Locate every blood parasite and identify its species.
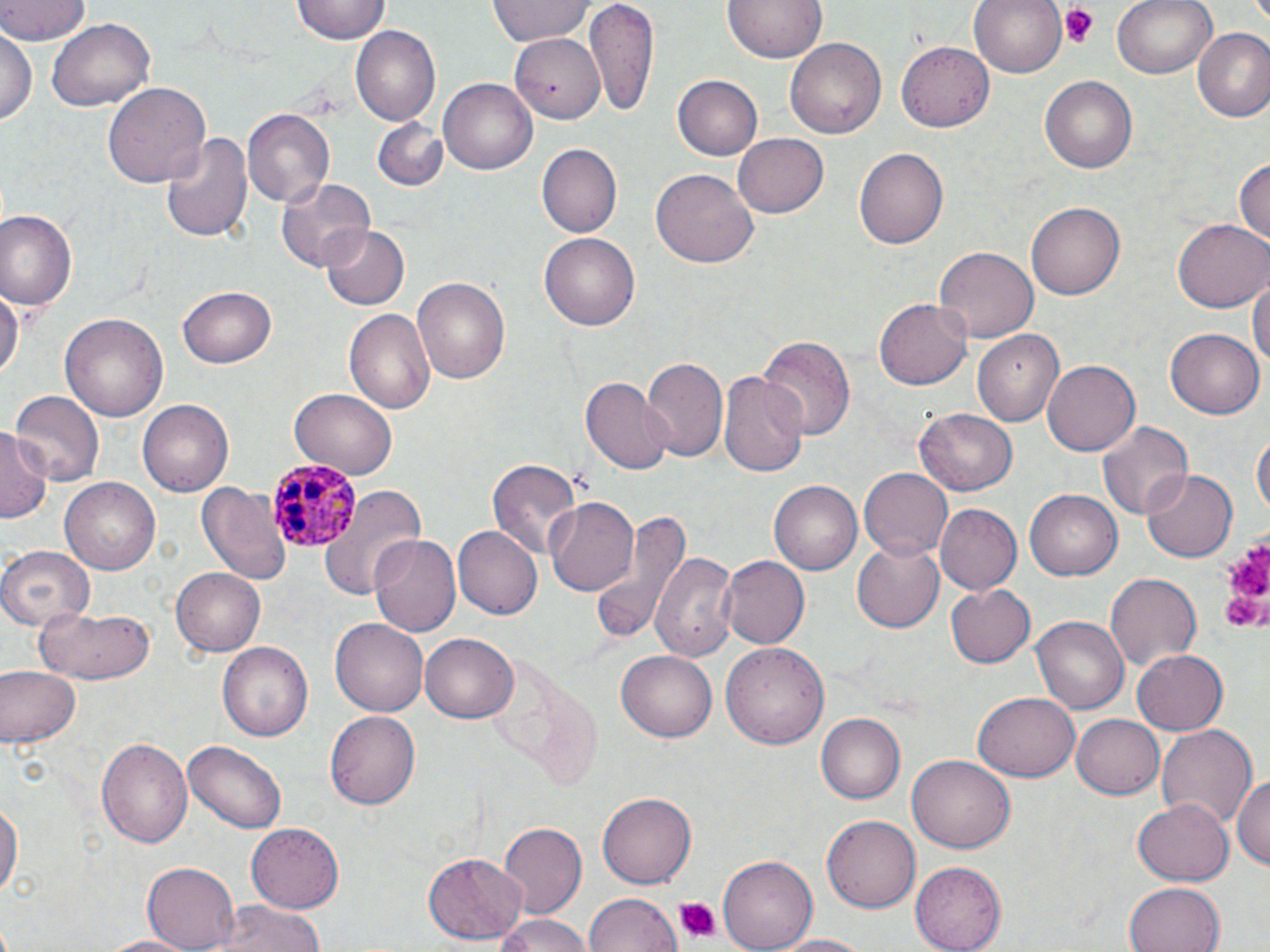

Approximate bounding boxes as (x1, y1, x2, y2) in pixels.
Plasmodium malariae-infected red blood cells: (268, 459, 363, 552).
No Plasmodium falciparum, Plasmodium ovale, Plasmodium vivax, Babesia divergens, or Trypanosoma brucei observed.

Platelet locations: (1062, 6, 1101, 46), (1217, 530, 1270, 638), (671, 895, 721, 942). Uninfected red blood cell locations: (0, 0, 92, 46), (292, 0, 390, 44), (488, 0, 592, 46), (584, 0, 659, 115), (721, 0, 828, 64), (969, 0, 1069, 79), (1113, 0, 1218, 79), (46, 17, 154, 112), (1, 24, 36, 132), (351, 26, 440, 126), (1192, 27, 1270, 123), (511, 35, 598, 124), (784, 37, 885, 140), (899, 40, 993, 131), (675, 74, 763, 160), (1041, 75, 1135, 174), (439, 78, 537, 175), (102, 82, 212, 191), (241, 109, 337, 207), (371, 118, 450, 192), (162, 128, 254, 244), (731, 134, 832, 217), (535, 143, 621, 237), (853, 147, 948, 250), (1233, 154, 1269, 250), (652, 169, 757, 270), (275, 175, 374, 272), (1025, 201, 1124, 302), (1, 210, 78, 309), (1173, 218, 1270, 313), (318, 222, 409, 309), (542, 232, 638, 331), (934, 245, 1039, 343), (1250, 271, 1270, 379), (412, 274, 511, 387), (0, 282, 21, 383), (178, 286, 276, 369), (874, 298, 972, 391), (343, 306, 436, 418), (60, 312, 169, 422), (1166, 327, 1263, 418), (973, 330, 1064, 426), (758, 334, 854, 440), (641, 356, 728, 465), (1041, 360, 1138, 458), (720, 368, 810, 480), (582, 376, 673, 474), (289, 387, 397, 479), (9, 390, 104, 488), (136, 399, 233, 496), (917, 406, 1020, 497), (1096, 420, 1193, 522), (0, 427, 49, 524), (1253, 429, 1269, 525), (487, 456, 580, 561), (1143, 467, 1238, 563), (860, 469, 953, 558), (60, 477, 161, 574), (771, 480, 862, 576), (196, 481, 290, 588), (320, 486, 428, 601), (1025, 489, 1123, 580), (546, 496, 639, 596), (934, 503, 1021, 595), (590, 507, 688, 647), (454, 525, 542, 619), (369, 533, 462, 640), (850, 539, 944, 633), (0, 545, 93, 629), (650, 548, 741, 663), (718, 555, 812, 649), (171, 566, 266, 656), (1106, 574, 1199, 671), (947, 585, 1035, 667), (31, 604, 157, 683), (1032, 614, 1127, 714), (330, 616, 429, 715), (420, 633, 517, 723), (218, 641, 312, 742), (723, 642, 830, 751), (1132, 649, 1228, 735), (615, 650, 716, 743), (0, 667, 79, 748), (974, 691, 1079, 782), (326, 707, 420, 806), (816, 713, 905, 803), (1070, 714, 1164, 800), (1155, 722, 1259, 830), (97, 738, 193, 848), (183, 739, 287, 832), (1211, 741, 1270, 854), (907, 755, 1013, 855), (1232, 771, 1270, 874), (0, 794, 22, 906), (597, 794, 694, 888), (1133, 798, 1234, 884), (824, 813, 922, 912), (498, 821, 588, 915), (246, 824, 342, 914), (424, 851, 527, 944), (718, 854, 817, 952), (912, 862, 1006, 951), (142, 863, 239, 950), (1124, 880, 1227, 952), (584, 893, 681, 952), (195, 901, 328, 952), (491, 914, 595, 952), (769, 933, 877, 952), (94, 934, 202, 952). Slide-level diagnosis: Plasmodium malariae. Optical microscopy. Thin blood smear. One field of a larger specimen. Image is 1270×952 pixels. 1000x magnification. May-Grünwald-Giemsa-stained preparation.